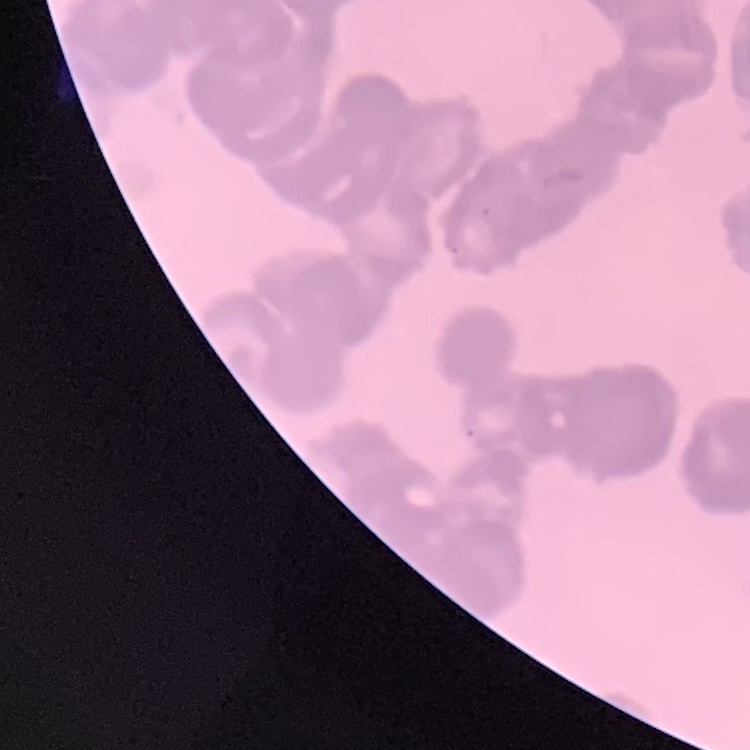

The erythrocytes exhibit rouleaux formation. Thin peripheral smear. Square crop of a larger photomicrograph. Field's or Giemsa stain.